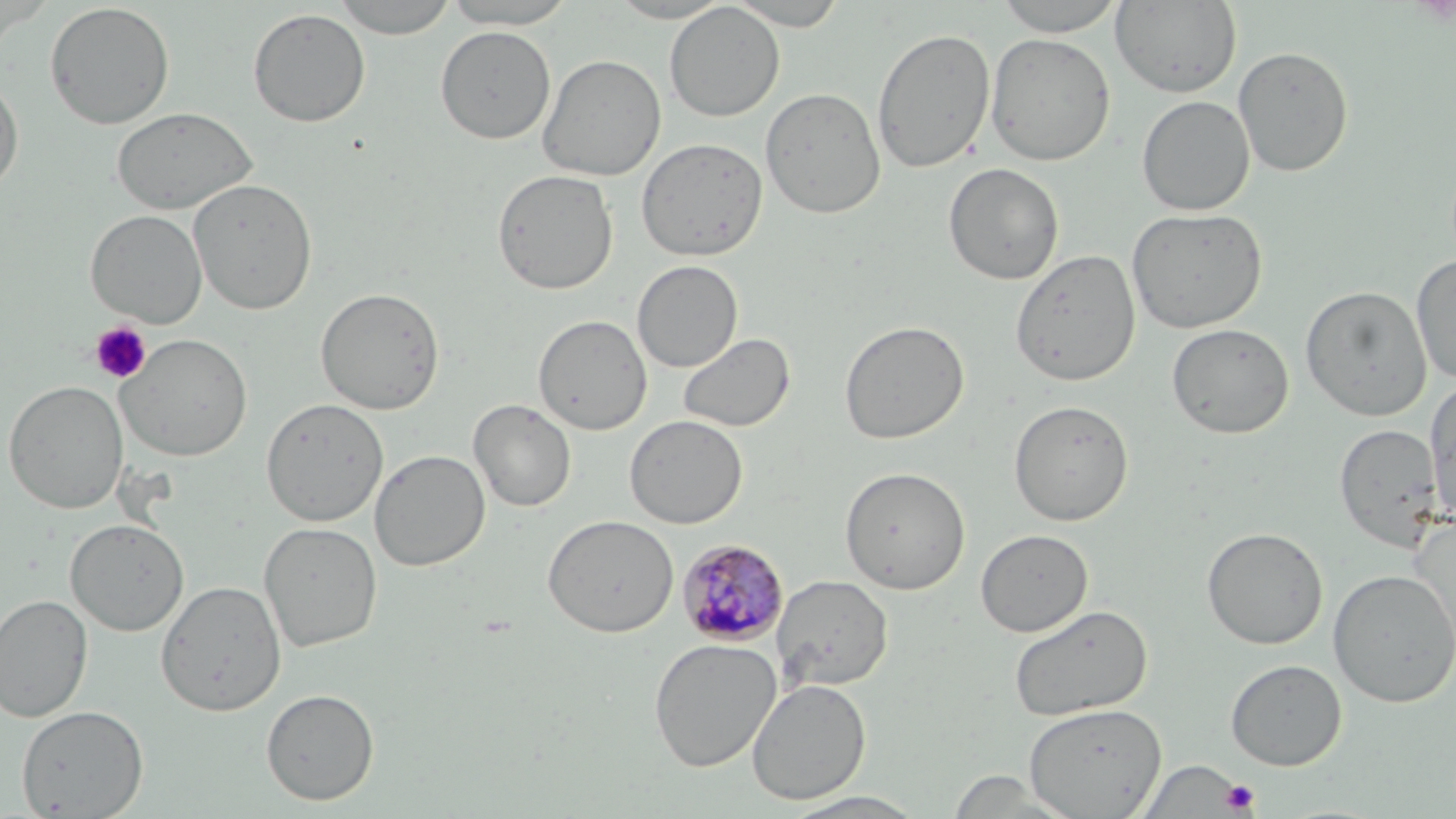

Summary:
  - Coordinate format: approximate bounding boxes as (x1, y1, x2, y2) in pixels
  - Uninfected red blood cell locations: (331, 0, 461, 38), (437, 0, 583, 29), (603, 0, 737, 23), (725, 0, 851, 30), (992, 0, 1128, 36), (1111, 0, 1241, 98), (664, 2, 785, 122), (44, 3, 175, 129), (247, 8, 371, 127), (435, 26, 556, 144), (871, 26, 996, 173), (985, 32, 1116, 166), (1232, 45, 1354, 177), (538, 54, 666, 181), (0, 74, 24, 195), (760, 87, 886, 219), (1137, 95, 1255, 216), (111, 106, 258, 216), (636, 137, 768, 262), (943, 162, 1064, 285), (492, 169, 619, 295), (188, 177, 318, 314), (1126, 207, 1268, 334), (85, 209, 207, 327), (1010, 249, 1141, 387), (1411, 254, 1456, 384), (632, 260, 743, 373), (1300, 285, 1433, 421), (315, 287, 445, 415), (533, 315, 652, 434), (839, 319, 969, 445), (1167, 322, 1294, 439), (677, 332, 796, 433), (116, 333, 253, 461), (1425, 378, 1456, 525), (3, 380, 128, 514), (261, 398, 389, 527), (468, 399, 577, 512), (1008, 399, 1134, 526), (624, 414, 748, 529), (1334, 422, 1446, 553), (370, 449, 490, 571), (839, 465, 970, 595), (543, 514, 679, 637), (1407, 514, 1456, 659), (65, 518, 189, 635), (259, 522, 383, 652), (1201, 526, 1329, 650), (975, 529, 1093, 636), (1328, 569, 1456, 708), (771, 574, 894, 692), (155, 580, 286, 717), (0, 594, 93, 722), (1009, 603, 1153, 721), (648, 638, 782, 772), (1225, 659, 1347, 770), (746, 678, 872, 805), (261, 688, 380, 806), (1024, 703, 1167, 818), (16, 704, 149, 818), (1137, 761, 1246, 817), (944, 770, 1081, 818), (780, 791, 930, 818)
  - Platelet locations: (89, 321, 152, 384), (1219, 779, 1260, 815)
  - Plasmodium malariae-infected red blood cell locations: (677, 539, 790, 647)
  - Slide-level diagnosis: Plasmodium malariae
  - Stain: May-Grünwald-Giemsa
  - Image size: 1456×819 pixels
  - Preparation: thin blood film
  - Modality: light microscopy
  - Field of view: one of a larger specimen
  - Magnification: 1000x